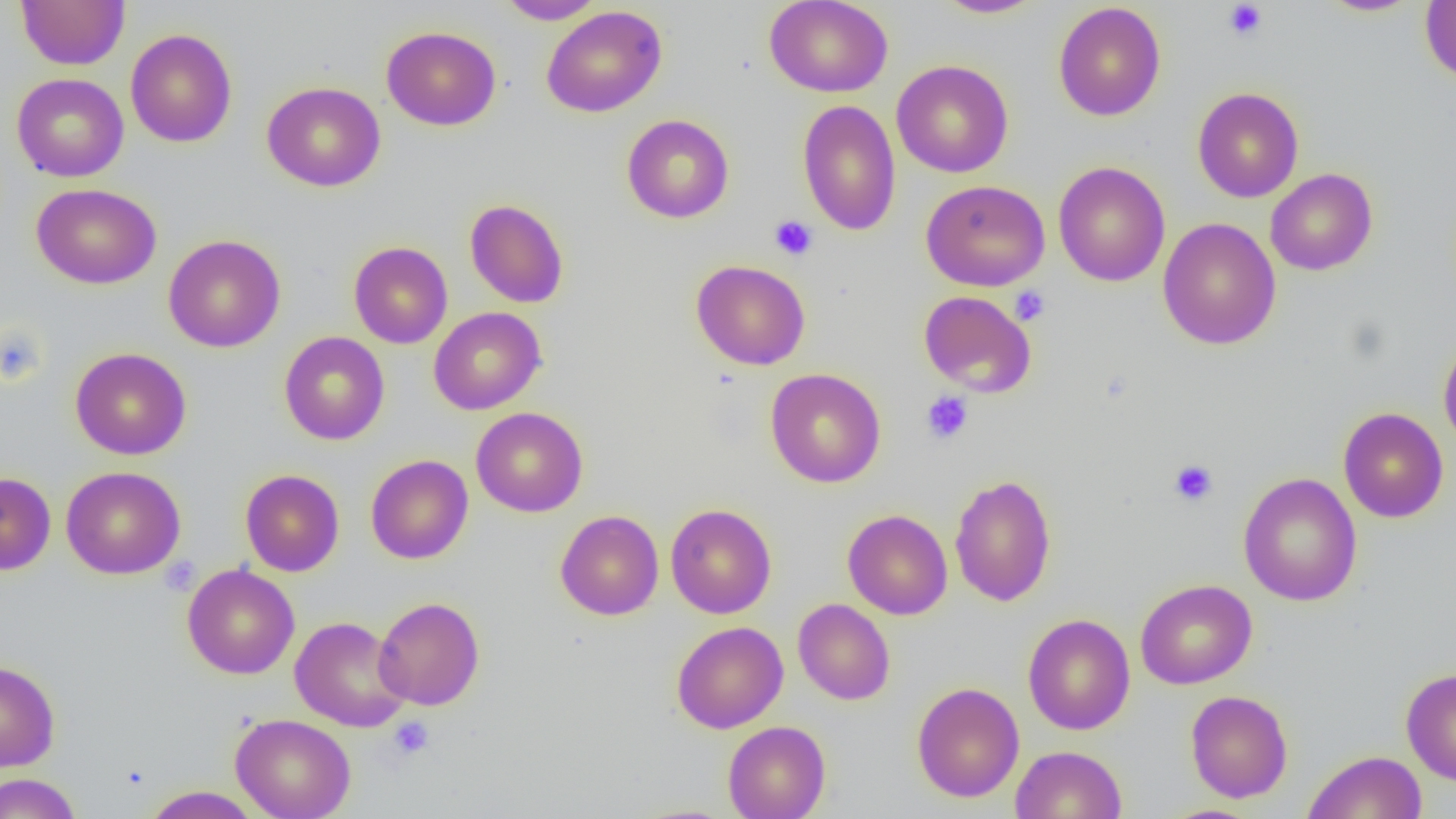

Summary:
  - Coordinate format: approximate bounding boxes as (x1, y1, x2, y2) in pixels
  - Platelet locations: (1223, 1, 1268, 42), (769, 215, 818, 260), (1009, 286, 1050, 325), (0, 326, 47, 386), (920, 391, 974, 445), (1169, 459, 1219, 506), (388, 716, 434, 761)
  - Uninfected red blood cell locations: (16, 0, 129, 70), (495, 0, 606, 24), (764, 0, 893, 98), (933, 0, 1046, 19), (1317, 0, 1423, 17), (1420, 1, 1456, 82), (1053, 2, 1166, 121), (541, 6, 667, 117), (381, 26, 501, 131), (125, 28, 237, 148), (891, 60, 1013, 178), (11, 73, 129, 182), (262, 81, 386, 192), (1192, 87, 1304, 203), (797, 100, 901, 235), (621, 114, 734, 223), (1053, 161, 1171, 287), (1265, 168, 1378, 276), (921, 179, 1050, 291), (31, 183, 162, 289), (464, 199, 569, 308), (1158, 217, 1281, 350), (163, 234, 286, 352), (349, 241, 453, 348), (690, 259, 811, 370), (918, 290, 1037, 397), (429, 307, 546, 415), (279, 332, 390, 445), (1438, 337, 1456, 454), (70, 347, 191, 460), (765, 368, 886, 488), (471, 407, 588, 517), (1338, 407, 1449, 523), (365, 454, 474, 564), (61, 466, 186, 579), (240, 469, 344, 576), (1238, 471, 1363, 607), (0, 472, 56, 575), (949, 473, 1057, 607), (665, 503, 776, 619), (842, 509, 953, 620), (555, 510, 664, 620), (182, 563, 300, 679), (1135, 579, 1257, 689), (374, 596, 485, 710), (793, 598, 895, 705), (1023, 613, 1136, 735), (289, 616, 410, 732), (671, 621, 788, 734), (0, 660, 60, 772), (1401, 667, 1456, 785), (911, 682, 1025, 803), (1185, 690, 1293, 803), (231, 713, 356, 819), (723, 721, 830, 819), (1011, 745, 1127, 819), (1303, 750, 1427, 819), (0, 773, 82, 819), (141, 786, 262, 818)
  - Slide-level diagnosis: no evidence of blood parasites
  - Image size: 1456×819 pixels
  - Modality: optical microscopy
  - Magnification: 1000x
  - Field of view: one of a larger specimen
  - Preparation: thin blood smear